Give the position of every malaria parasite.
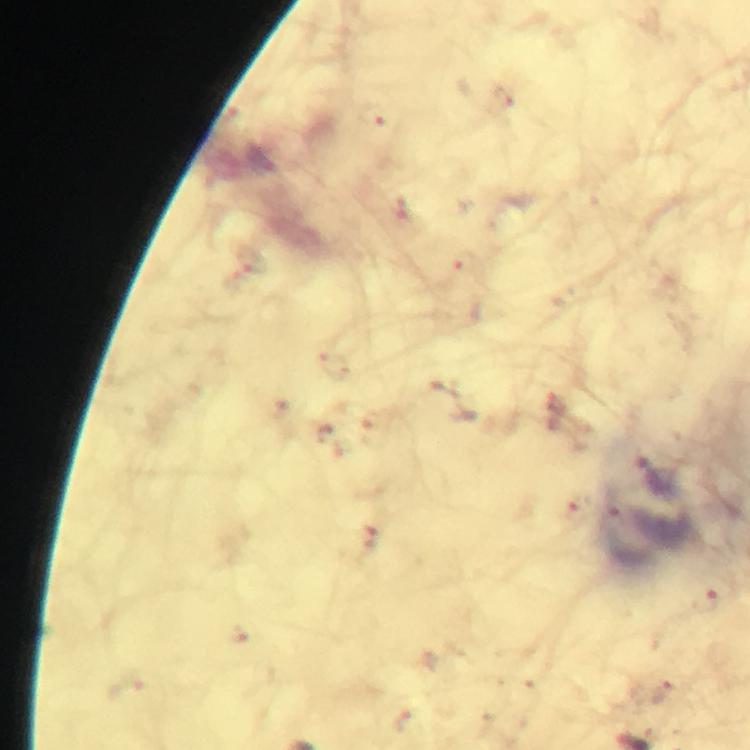
Approximate centers as {x, y} in pixels.
Malaria parasites: {375, 114}, {399, 208}.

{
  "image_size": "750×750 pixels",
  "preparation": "thick blood smear",
  "cropped_from": "one field of view",
  "context": "from a malaria diagnostic workup",
  "immersion_oil": "applied",
  "magnification": "100x",
  "stain": "Giemsa",
  "capture": "smartphone mounted on the microscope"
}